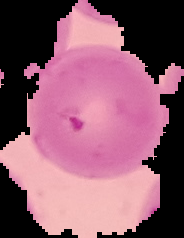

image_type: segmented cell region on a black background
result: Plasmodium parasites identified
preparation: thin blood smear
image_size: 184×238 pixels